Name the parasite shown.
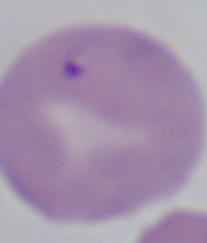

Babesia.

Summary:
  - Magnification: 1000x
  - Modality: micrograph